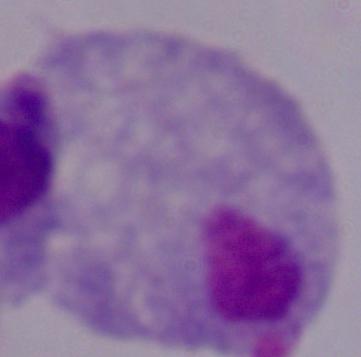

{
  "magnification": "1000x",
  "identification": "trichomonad",
  "modality": "micrograph"
}